Name the cell type shown.
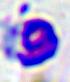
A leukocyte.

Summary:
  - Magnification: 400x
  - Modality: micrograph